Report the malaria status of this cell.
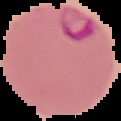
Parasitized.

{
  "preparation": "thin blood film",
  "image_size": "121×121 pixels",
  "image_type": "segmented cell region with the area outside set to black"
}